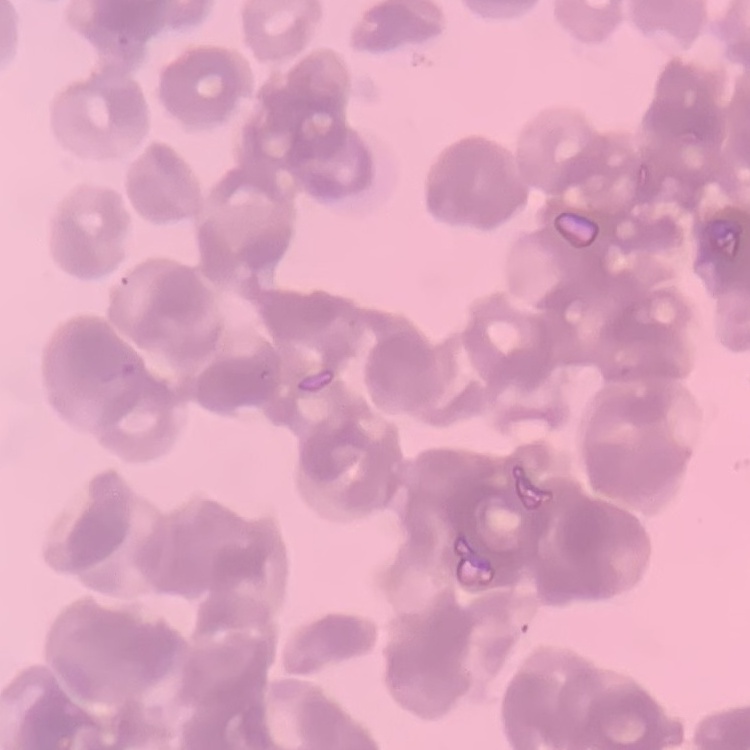

{
  "red_blood_cell_morphology": "rouleaux formation",
  "preparation": "thin blood smear",
  "stain": "Field's or Giemsa",
  "image_type": "one tile cut from a larger photomicrograph"
}